Identify the parasite.
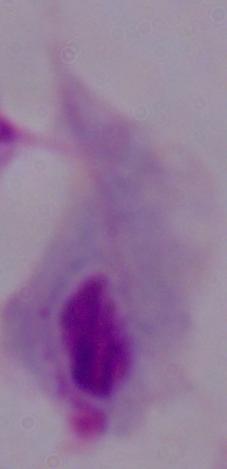
A trichomonad.

Summary:
  - Magnification: 1000x
  - Modality: micrograph